Give the preparation type.
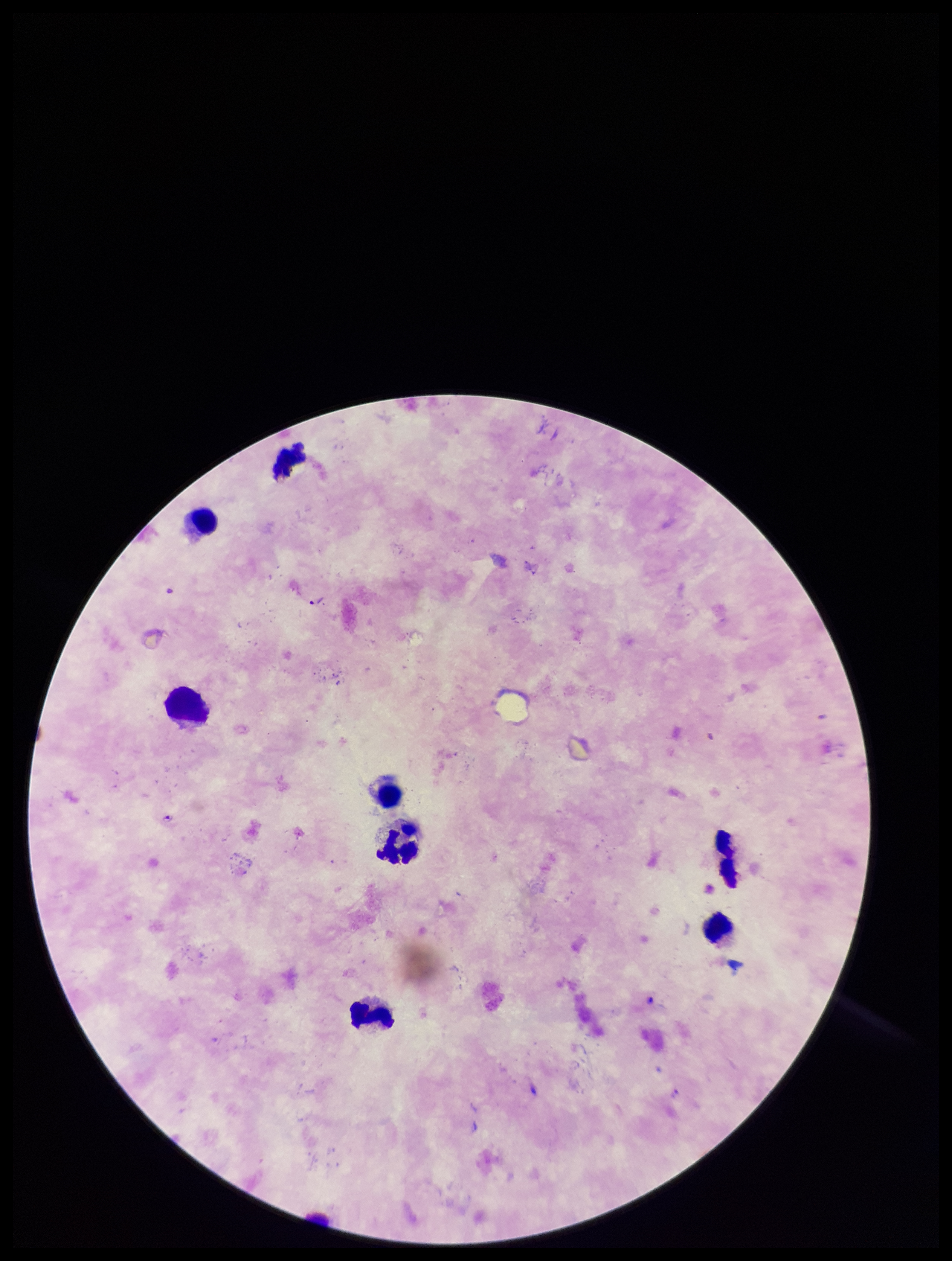

A thick smear.

stain = Giemsa
parasite count = 2
image size = 952×1261 pixels
species reported for this patient = Plasmodium falciparum
Plasmodium parasites = detected
leukocyte count = 8
field of view = single
patient malaria status = positive
capture = smartphone photograph through the microscope eyepiece